Report the malaria status of this cell.
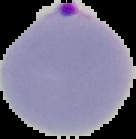
Parasitized.

{
  "image_type": "segmented cell region with the area outside set to black",
  "image_size": "136×139 pixels",
  "preparation": "thin blood film"
}